Give the location of every parasitized RBC.
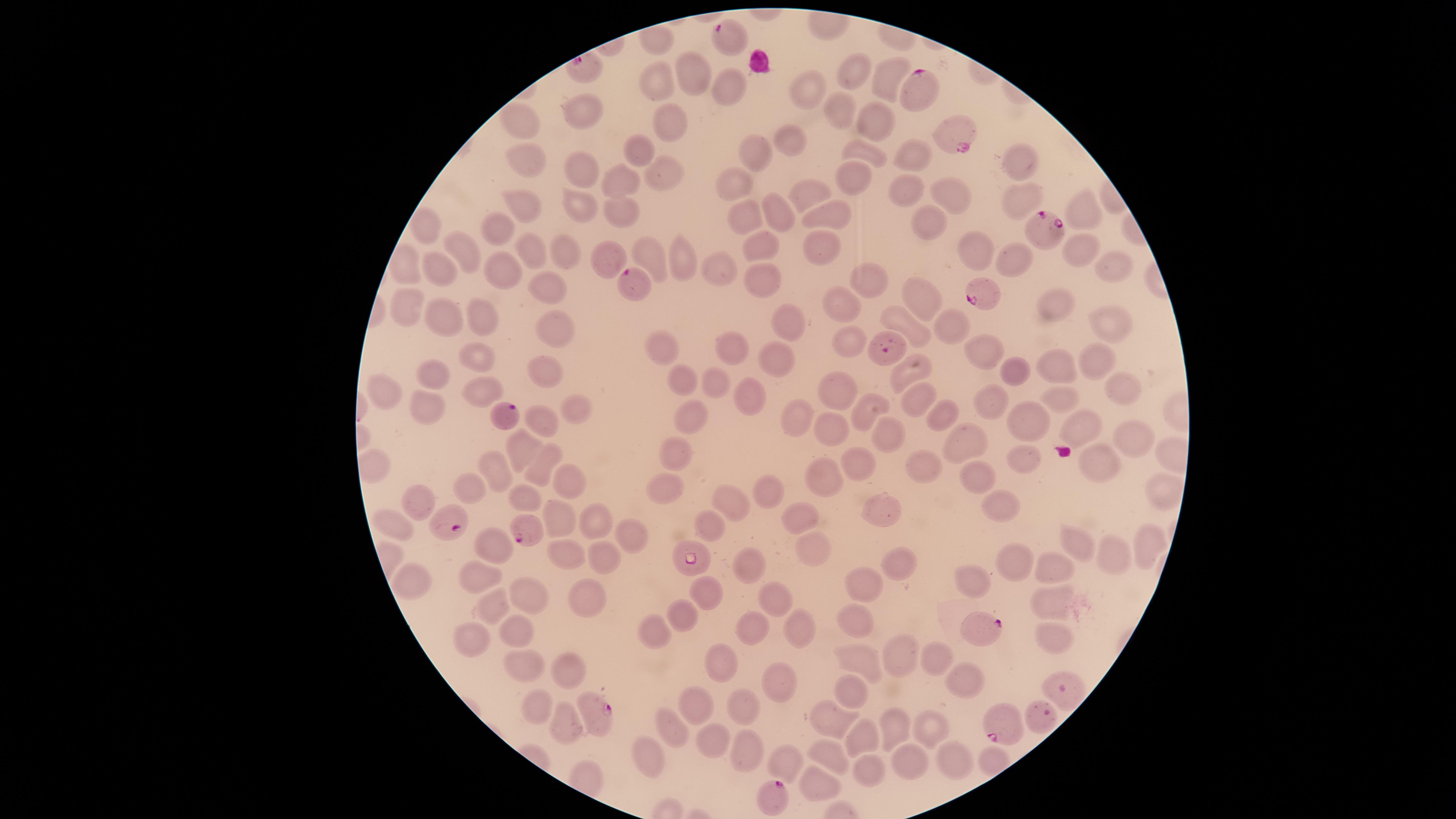

Approximate marker points as {x, y} in pixels.
Parasitized RBCs: {913, 86}, {955, 133}, {1046, 226}, {632, 281}, {980, 295}, {505, 414}, {450, 521}, {525, 532}, {690, 562}, {979, 626}, {599, 710}, {1001, 726}, {772, 794}.

Approximate marker points as {x, y} in pixels. Uninfected RBCs: {695, 71}, {854, 72}, {889, 75}, {656, 81}, {728, 87}, {809, 91}, {833, 108}, {583, 109}, {872, 117}, {671, 120}, {519, 125}, {789, 140}, {639, 149}, {863, 150}, {755, 152}, {912, 153}, {1017, 159}, {529, 163}, {656, 171}, {858, 175}, {577, 176}, {734, 184}, {618, 185}, {904, 189}, {806, 190}, {946, 191}, {1022, 191}, {577, 194}, {519, 204}, {612, 207}, {775, 209}, {748, 213}, {1082, 213}, {831, 215}, {931, 222}, {424, 225}, {496, 225}, {817, 243}, {760, 245}, {973, 246}, {530, 247}, {1070, 248}, {460, 249}, {562, 254}, {686, 257}, {649, 258}, {613, 259}, {1015, 261}, {1113, 261}, {503, 267}, {439, 268}, {718, 268}, {869, 277}, {763, 278}, {539, 282}, {918, 291}, {839, 301}, {1049, 305}, {405, 312}, {786, 317}, {898, 318}, {445, 320}, {1104, 320}, {474, 321}, {948, 323}, {558, 327}, {855, 339}, {650, 342}, {734, 346}, {977, 346}, {778, 353}, {477, 356}, {1094, 359}, {1054, 363}, {1017, 366}, {545, 371}, {902, 373}, {432, 375}, {681, 377}, {715, 379}, {1126, 387}, {477, 391}, {836, 392}, {380, 393}, {755, 394}, {916, 396}, {1060, 396}, {990, 400}, {579, 406}, {943, 409}, {427, 410}, {870, 410}, {690, 414}, {796, 415}, {1028, 415}, {540, 420}, {1086, 431}, {839, 432}, {1132, 435}, {884, 438}, {967, 443}, {524, 447}, {672, 452}, {851, 455}, {1021, 458}, {1102, 458}, {497, 464}, {926, 468}, {542, 469}, {969, 473}, {564, 476}, {815, 481}, {669, 486}, {1162, 487}, {476, 490}, {764, 493}, {521, 496}, {416, 500}, {731, 501}, {994, 501}, {882, 509}, {560, 514}, {594, 517}, {804, 518}, {391, 524}, {707, 524}, {632, 534}, {497, 539}, {1079, 540}, {1142, 540}, {560, 547}, {812, 548}, {1109, 556}, {607, 557}, {1016, 560}, {745, 561}, {897, 564}, {1055, 567}, {471, 576}, {411, 577}, {973, 578}, {857, 584}, {709, 590}, {589, 595}, {528, 596}, {490, 601}, {769, 601}, {1050, 602}, {855, 613}, {680, 614}, {803, 623}, {752, 630}, {515, 631}, {653, 632}, {470, 636}, {1049, 638}, {899, 649}, {930, 657}, {859, 658}, {521, 662}, {561, 663}, {723, 664}, {976, 677}, {779, 683}, {857, 689}, {742, 701}, {700, 703}, {537, 710}, {826, 720}, {564, 722}, {895, 726}, {929, 726}, {669, 728}, {855, 734}, {713, 736}, {747, 746}, {826, 751}, {651, 755}, {955, 755}, {908, 762}, {785, 764}, {872, 772}, {816, 785}. Species: Plasmodium falciparum. Image is 1456×819 pixels. Thin smear of blood. Smartphone photograph through the microscope eyepiece. The visible region is circular. Giemsa-stained preparation. Single field of view.